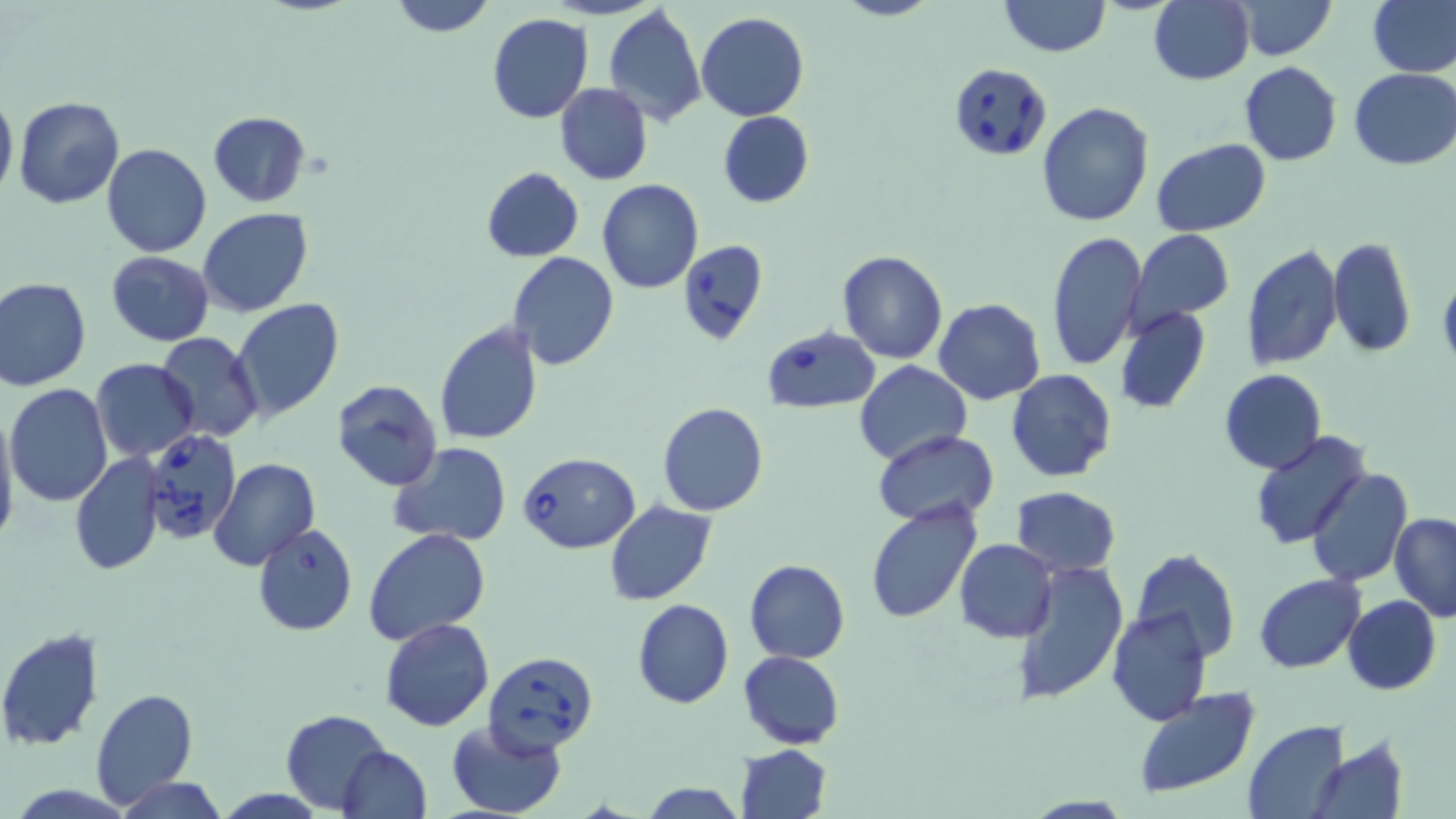

slide-level diagnosis = Babesia divergens
modality = optical microscopy
preparation = thin blood film
field of view = single
uninfected red blood cell locations = approximate bounding boxes as (x1, y1, x2, y2) in pixels: (387, 0, 497, 37), (833, 0, 937, 22), (1150, 0, 1254, 85), (1236, 0, 1336, 60), (1369, 0, 1456, 77), (998, 1, 1111, 57), (603, 5, 707, 126), (696, 12, 809, 122), (488, 13, 594, 124), (1238, 62, 1342, 165), (1349, 68, 1456, 169), (554, 82, 653, 185), (0, 88, 17, 201), (13, 96, 124, 209), (1037, 101, 1154, 227), (718, 110, 814, 208), (207, 111, 310, 207), (1152, 139, 1271, 235), (102, 142, 211, 258), (481, 166, 583, 263), (597, 179, 703, 293), (197, 207, 313, 317), (1131, 230, 1234, 324), (1045, 231, 1147, 372), (1327, 237, 1416, 358), (1241, 244, 1344, 371), (836, 250, 949, 364), (105, 252, 215, 345), (506, 253, 620, 371), (1438, 266, 1456, 372), (0, 276, 91, 390), (229, 298, 343, 423), (933, 299, 1046, 404), (1114, 305, 1210, 414), (432, 320, 544, 445), (154, 333, 264, 442), (91, 360, 200, 462), (855, 361, 971, 467), (1006, 369, 1117, 483), (1220, 369, 1325, 474), (330, 379, 444, 492), (5, 383, 113, 507), (656, 402, 770, 517), (0, 406, 20, 555), (874, 431, 998, 524), (1249, 433, 1368, 551), (389, 441, 514, 547), (69, 452, 164, 575), (208, 458, 321, 570), (1305, 467, 1412, 587), (1013, 487, 1121, 577), (604, 500, 718, 605), (864, 501, 982, 626), (1388, 511, 1456, 622), (252, 523, 357, 636), (364, 526, 490, 646), (954, 538, 1057, 642), (1132, 548, 1238, 664), (745, 558, 849, 663), (1011, 562, 1129, 706), (1254, 574, 1364, 673), (1343, 595, 1440, 695), (631, 598, 733, 709), (1106, 606, 1213, 728), (380, 619, 493, 732), (0, 630, 106, 750), (738, 649, 844, 748), (1132, 686, 1261, 800), (89, 687, 198, 808), (282, 710, 390, 811), (444, 718, 567, 819), (1245, 720, 1349, 819), (1312, 738, 1406, 819), (734, 743, 833, 819), (338, 747, 432, 819), (115, 776, 228, 819), (639, 781, 748, 818)
magnification = 1000x
Babesia divergens-infected red blood cell locations = approximate bounding boxes as (x1, y1, x2, y2) in pixels: (950, 63, 1049, 158), (678, 239, 767, 346), (762, 325, 881, 414), (142, 430, 242, 545), (517, 451, 640, 553), (483, 650, 598, 756)
image size = 1456×819 pixels
stain = May-Grünwald-Giemsa